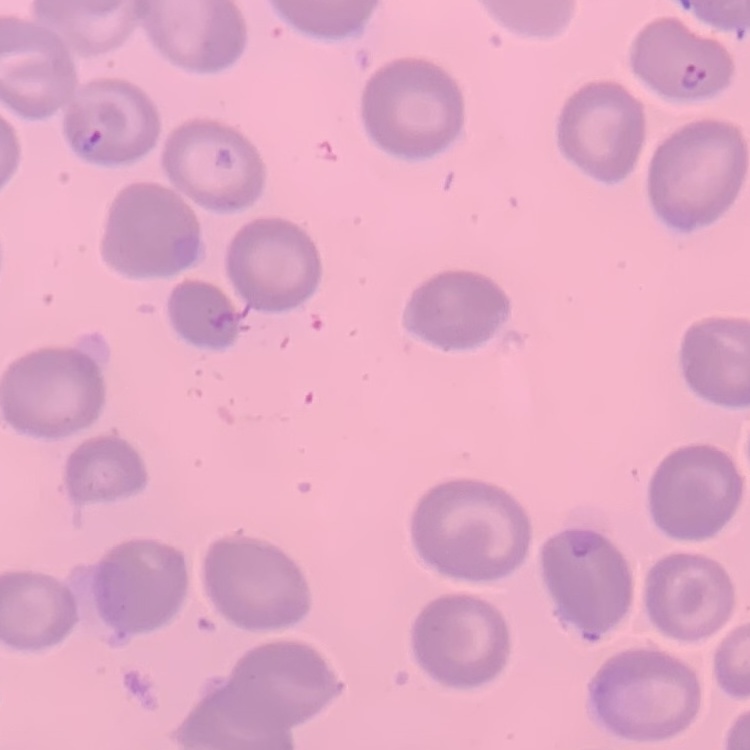

The red blood cells show no rouleaux formation. Stained with either Field's or Giemsa. Thin blood film. One tile cut from a larger photomicrograph.